Name the parasite shown.
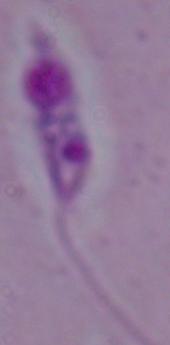

This is Leishmania.

Summary:
  - Modality: photomicrograph
  - Magnification: 1000x